Give the extent of all Trypanosoma brucei.
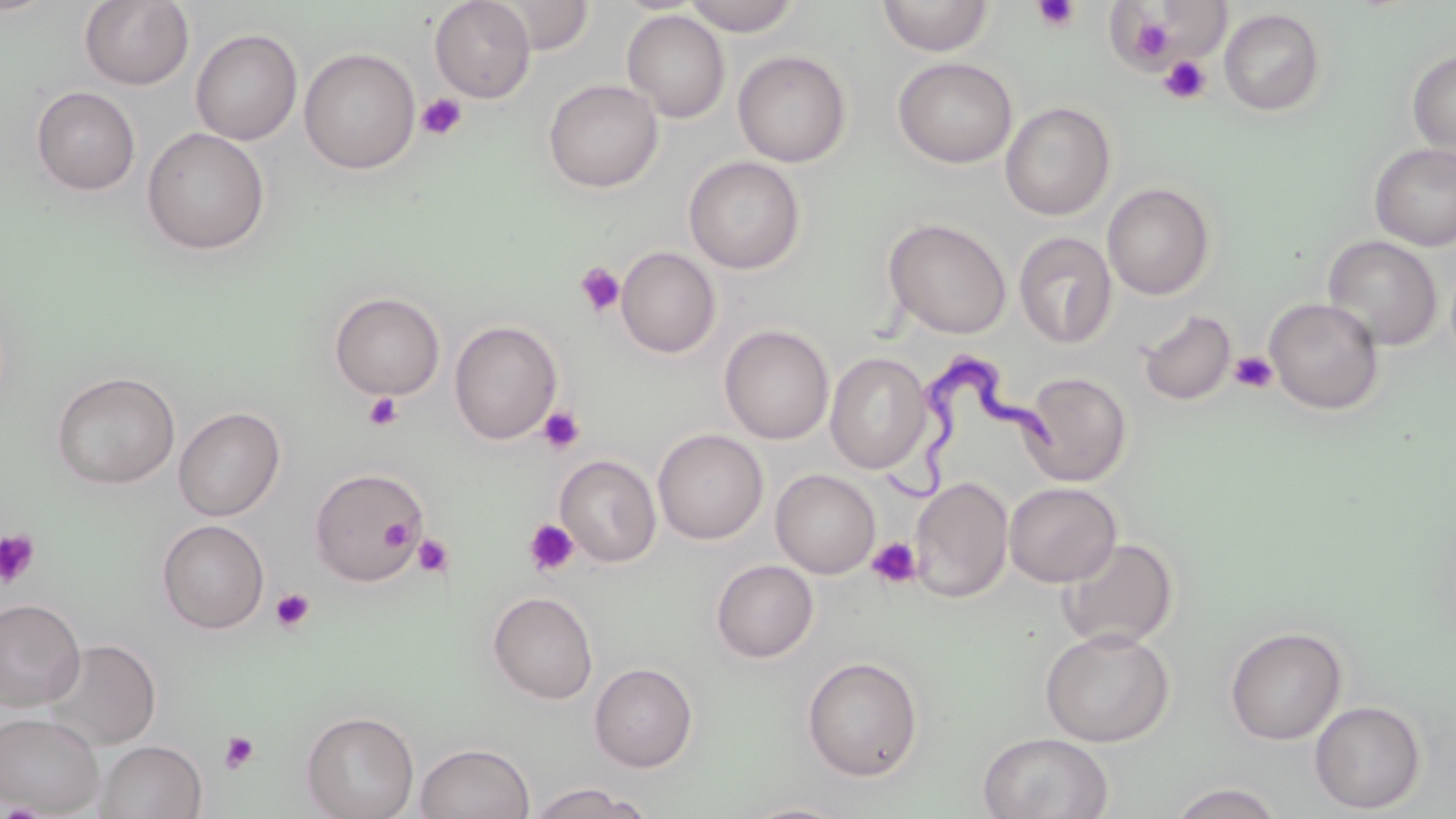

Approximate bounding boxes as named x1/y1/x2/y2 corners in pixels.
Trypanosoma brucei: (x1=877, y1=338, x2=1063, y2=505).

Uninfected red blood cell locations: (x1=430, y1=0, x2=535, y2=103), (x1=491, y1=0, x2=595, y2=55), (x1=683, y1=0, x2=801, y2=36), (x1=876, y1=0, x2=995, y2=57), (x1=79, y1=1, x2=194, y2=90), (x1=1219, y1=8, x2=1326, y2=116), (x1=622, y1=9, x2=730, y2=123), (x1=190, y1=28, x2=303, y2=146), (x1=299, y1=47, x2=420, y2=175), (x1=1406, y1=49, x2=1456, y2=159), (x1=733, y1=50, x2=851, y2=168), (x1=893, y1=57, x2=1017, y2=169), (x1=543, y1=79, x2=663, y2=193), (x1=31, y1=86, x2=141, y2=195), (x1=1000, y1=101, x2=1116, y2=220), (x1=141, y1=127, x2=270, y2=255), (x1=1369, y1=142, x2=1456, y2=251), (x1=683, y1=155, x2=805, y2=274), (x1=1102, y1=182, x2=1216, y2=300), (x1=883, y1=218, x2=1012, y2=340), (x1=1014, y1=231, x2=1117, y2=349), (x1=1322, y1=235, x2=1443, y2=351), (x1=616, y1=247, x2=721, y2=358), (x1=329, y1=291, x2=446, y2=400), (x1=1264, y1=297, x2=1384, y2=415), (x1=1138, y1=309, x2=1237, y2=406), (x1=449, y1=320, x2=562, y2=445), (x1=719, y1=324, x2=834, y2=444), (x1=825, y1=353, x2=933, y2=474), (x1=51, y1=371, x2=180, y2=489), (x1=1020, y1=372, x2=1132, y2=486), (x1=173, y1=406, x2=286, y2=521), (x1=653, y1=429, x2=768, y2=545), (x1=555, y1=455, x2=661, y2=567), (x1=309, y1=467, x2=427, y2=586), (x1=770, y1=469, x2=880, y2=578), (x1=908, y1=476, x2=1013, y2=603), (x1=1004, y1=482, x2=1121, y2=587), (x1=157, y1=519, x2=270, y2=634), (x1=1057, y1=537, x2=1179, y2=651), (x1=711, y1=560, x2=818, y2=663), (x1=487, y1=591, x2=598, y2=705), (x1=0, y1=598, x2=85, y2=712), (x1=1224, y1=625, x2=1347, y2=745), (x1=1039, y1=627, x2=1175, y2=747), (x1=42, y1=638, x2=162, y2=752), (x1=801, y1=656, x2=924, y2=782), (x1=589, y1=662, x2=698, y2=773), (x1=1309, y1=700, x2=1427, y2=814), (x1=301, y1=710, x2=419, y2=819), (x1=0, y1=712, x2=104, y2=816), (x1=978, y1=731, x2=1114, y2=818), (x1=95, y1=740, x2=207, y2=819), (x1=415, y1=742, x2=536, y2=819), (x1=1167, y1=782, x2=1285, y2=818), (x1=529, y1=783, x2=646, y2=818), (x1=736, y1=800, x2=857, y2=819). Platelet locations: (x1=1032, y1=0, x2=1081, y2=33), (x1=1129, y1=14, x2=1175, y2=61), (x1=1158, y1=56, x2=1212, y2=105), (x1=416, y1=93, x2=467, y2=141), (x1=574, y1=262, x2=625, y2=317), (x1=1230, y1=350, x2=1277, y2=394), (x1=362, y1=391, x2=403, y2=432), (x1=537, y1=406, x2=585, y2=454), (x1=378, y1=517, x2=415, y2=550), (x1=523, y1=518, x2=580, y2=576), (x1=0, y1=529, x2=40, y2=588), (x1=413, y1=533, x2=454, y2=578), (x1=866, y1=536, x2=922, y2=588), (x1=270, y1=587, x2=315, y2=633), (x1=219, y1=731, x2=259, y2=774). Slide-level diagnosis: Trypanosoma brucei. Captured at 1000x magnification. Optical microscopy. Single field of view. Image is 1456×819 pixels. Thin blood smear. May-Grünwald-Giemsa-stained preparation.